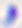

400x magnification. Toxoplasma gondii is shown. Photomicrograph.